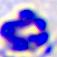

magnification = 400x
modality = micrograph
identification = white blood cell